Describe the morphology of the red blood cells.
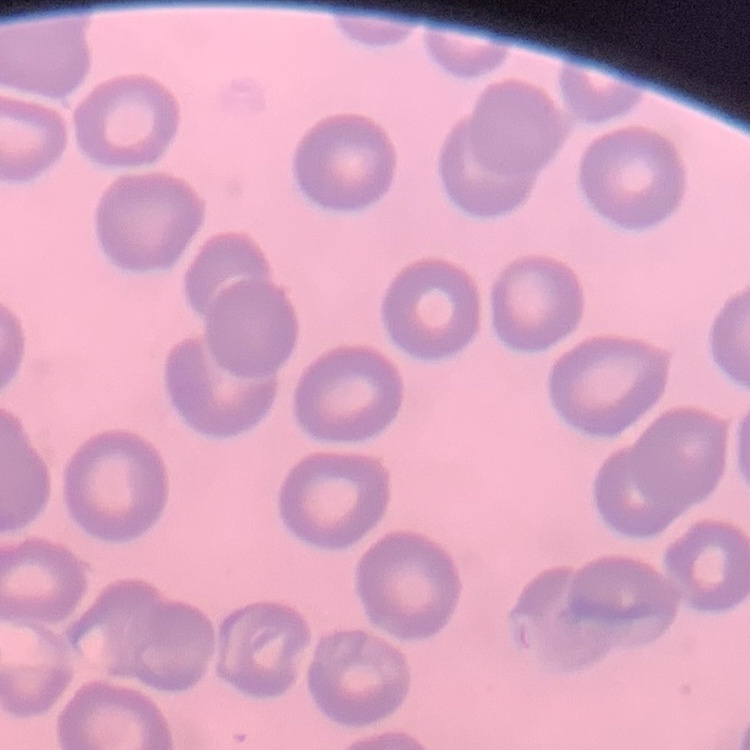

They show no rouleaux formation.

stain = Field's or Giemsa
image type = one tile cut from a larger photomicrograph
preparation = thin blood smear